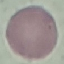 Malaria status: uninfected. Giemsa-stained preparation. Automatically extracted cell patch, resized to 64 × 64 pixels. Photographed with a smartphone camera at the microscope eyepiece. Thin blood smear.